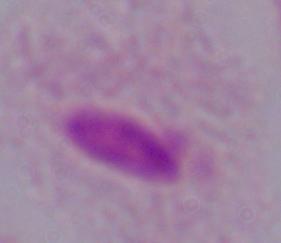
Summary:
  - Modality: photomicrograph
  - Magnification: 1000x
  - Identification: trichomonad